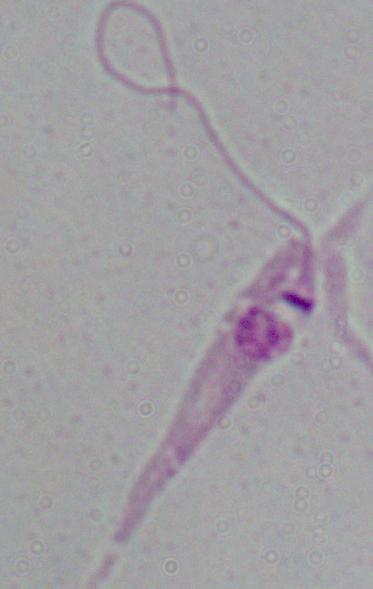

Summary:
  - Modality: photomicrograph
  - Identification: Leishmania
  - Magnification: 1000x